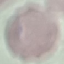
Result: no malaria parasites detected. Giemsa-stained preparation. Acquired by smartphone through the microscope eyepiece. Automatically extracted cell patch, resized to 64 × 64 pixels. Thin blood smear.